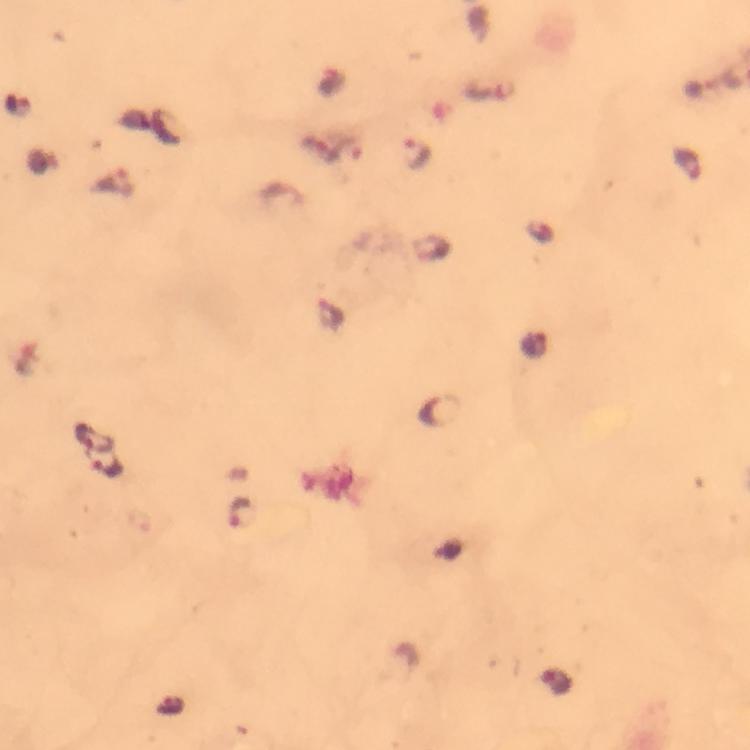 Approximate centers as {x, y} in pixels. Malaria parasite locations: {348, 152}, {415, 153}, {685, 163}, {333, 315}, {536, 346}, {444, 411}, {95, 437}, {109, 468}, {240, 513}, {554, 683}. Image is 750×750 pixels. Smartphone photograph taken through a microscope. Cropped region of a single field of view. Giemsa stain. 100x magnification. From a malaria diagnostic workup. Immersion oil applied. Thick blood film.